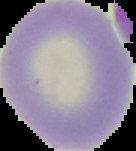
result = no malaria parasites detected
preparation = thin blood film
image size = 136×151 pixels
image type = cell region segmented out of the field of view; surrounding area masked to black